Assess the morphology of the red blood cells.
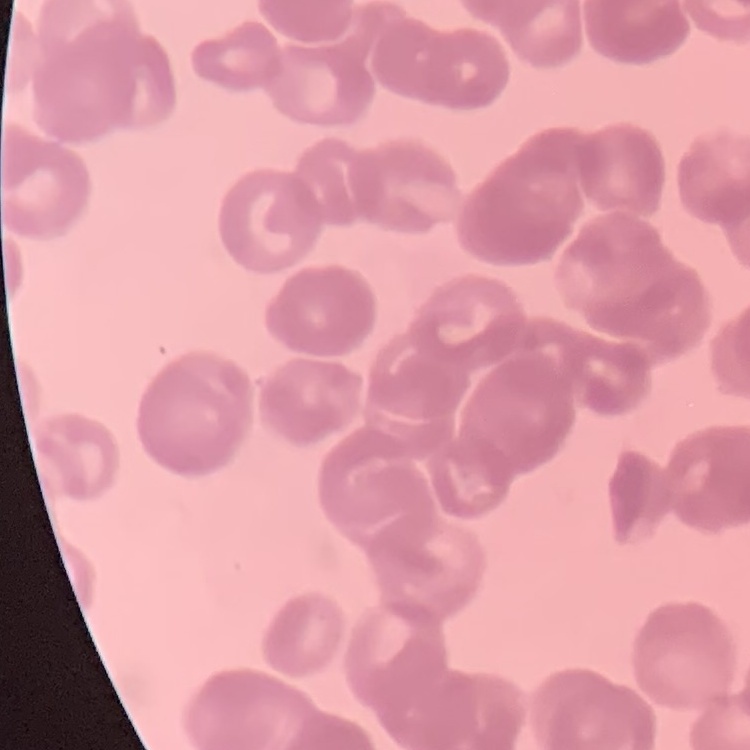

Rouleaux formation.

stain = Field's or Giemsa
preparation = thin blood smear
image type = one tile cut from a larger photomicrograph